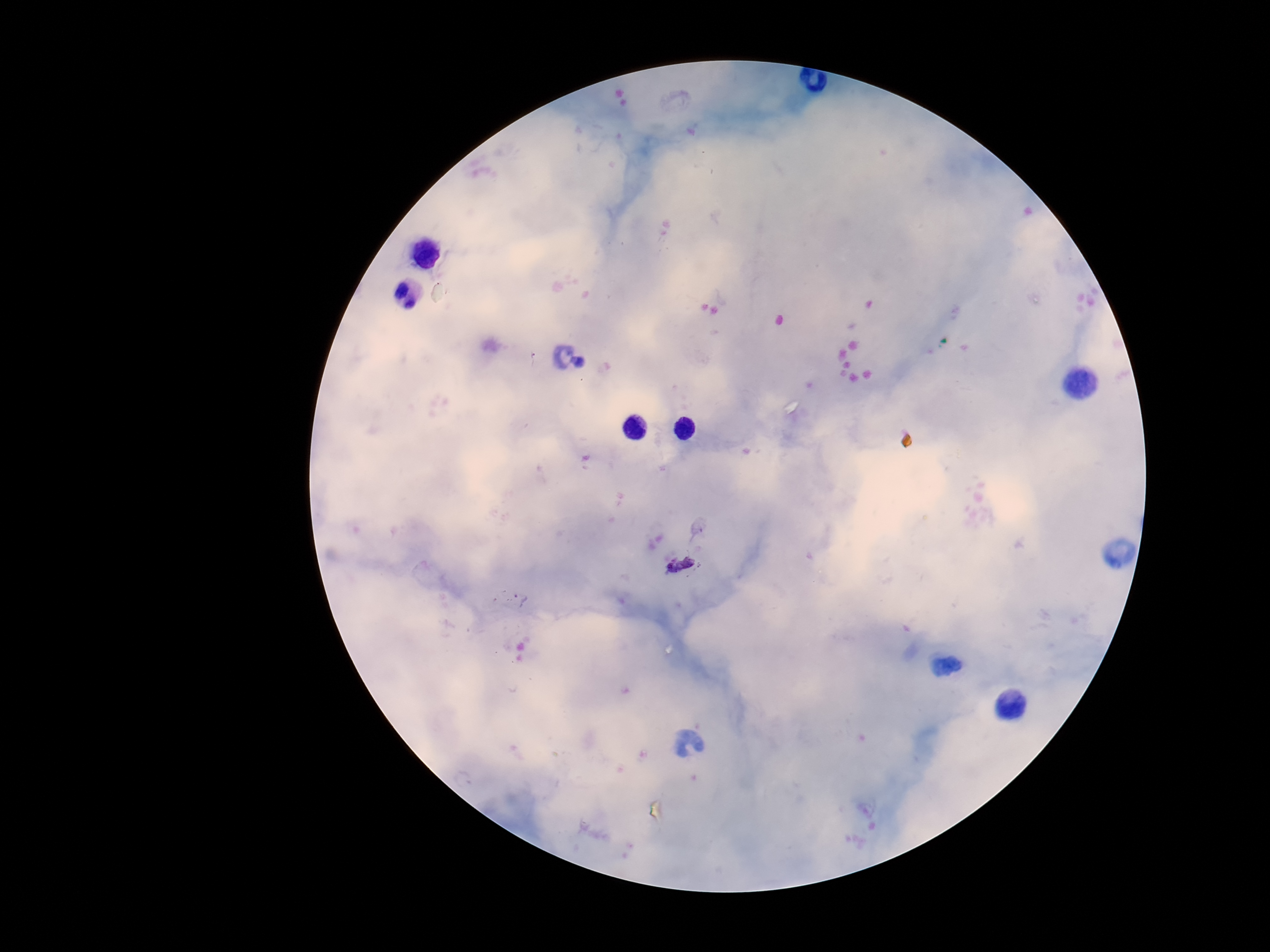
magnification = 100x
image size = 1270×952 pixels
patient malaria status = infected
stain = Giemsa
field of view = one from this slide
preparation = thick blood film
Plasmodium parasite locations = approximate centers as (x, y) in pixels: (679, 566), (518, 600)
capture = smartphone camera through the microscope eyepiece